Identify the parasite.
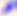

This is Toxoplasma gondii.

Summary:
  - Magnification: 400x
  - Modality: photomicrograph